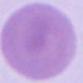

Summary:
  - Identification: erythrocyte
  - Modality: photomicrograph
  - Magnification: 1000x